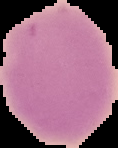

image_type: segmented cell region with the area outside set to black
result: no Plasmodium parasites seen
image_size: 118×148 pixels
preparation: thin blood smear